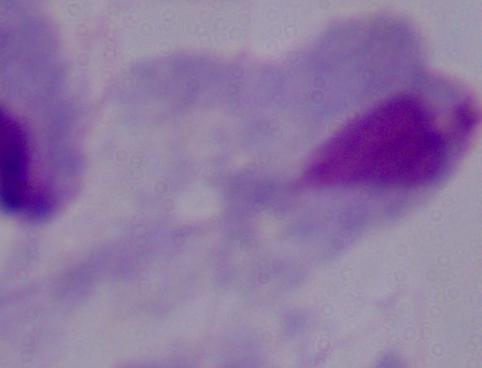
Summary:
  - Magnification: 1000x
  - Identification: trichomonad
  - Modality: photomicrograph